Name the parasite shown.
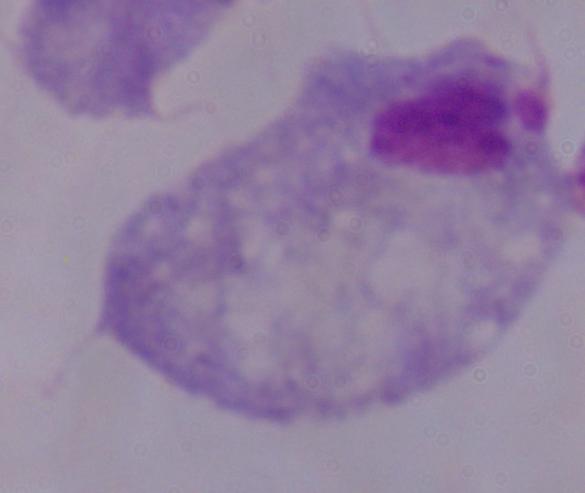
A trichomonad.

magnification = 1000x
modality = photomicrograph